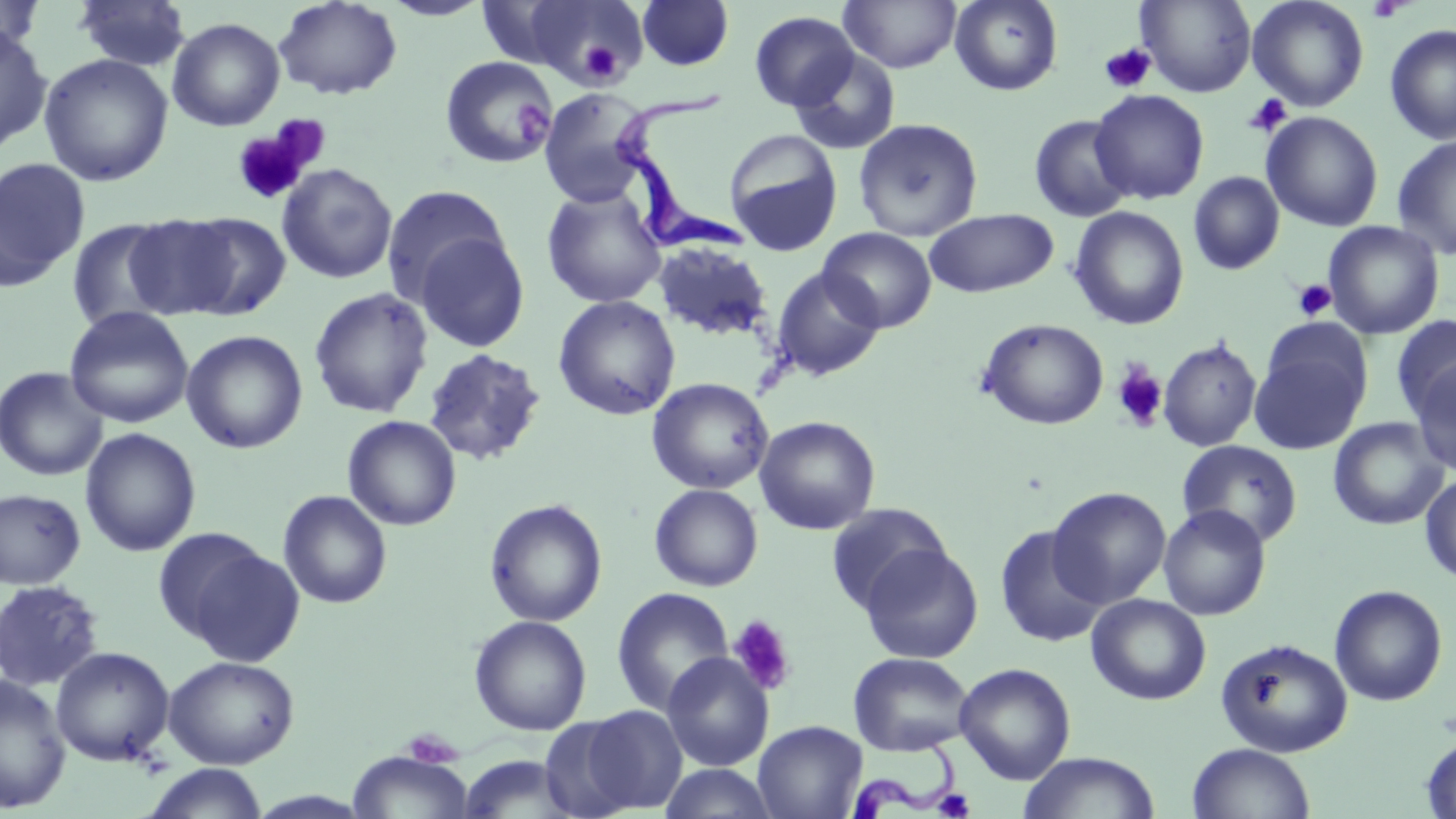
Approximate bounding boxes as (x1,y1)-(x2,y2) corner pairs in pixels. Platelet locations: (1366,0)-(1411,22), (575,38)-(623,83), (1099,44)-(1156,93), (1244,94)-(1291,137), (512,101)-(553,143), (231,121)-(320,206), (1292,279)-(1337,321), (1111,361)-(1168,432), (727,615)-(797,697), (932,788)-(976,818). Uninfected red blood cell locations: (0,0)-(43,61), (273,0)-(403,100), (380,0)-(494,20), (637,0)-(734,70), (839,0)-(962,74), (949,0)-(1063,96), (1136,0)-(1257,97), (1247,0)-(1369,112), (73,1)-(190,72), (523,2)-(648,90), (749,11)-(859,111), (167,17)-(285,132), (0,22)-(53,155), (1385,24)-(1456,144), (789,49)-(901,155), (39,53)-(174,186), (440,55)-(555,170), (538,87)-(653,207), (1090,89)-(1210,204), (1261,111)-(1384,232), (1029,115)-(1134,222), (853,118)-(983,241), (724,130)-(843,255), (1392,133)-(1456,261), (0,158)-(89,291), (276,164)-(397,284), (1188,171)-(1285,275), (381,185)-(512,306), (541,186)-(666,308), (1069,206)-(1190,330), (924,209)-(1058,298), (172,212)-(292,320), (128,217)-(240,321), (68,219)-(179,333), (1323,221)-(1444,340), (818,227)-(937,332), (411,230)-(530,353), (652,242)-(775,343), (771,266)-(885,382), (309,287)-(434,419), (553,295)-(680,420), (64,306)-(194,429), (1391,315)-(1456,424), (977,318)-(1109,430), (1260,318)-(1374,409), (181,330)-(308,454), (1157,338)-(1262,452), (1250,347)-(1366,455), (422,348)-(547,466), (1409,360)-(1456,476), (0,366)-(108,481), (646,377)-(774,494), (342,415)-(462,531), (754,416)-(880,535), (1328,417)-(1449,530), (80,427)-(201,557), (1177,439)-(1302,547), (1420,473)-(1456,585), (649,484)-(763,592), (1048,487)-(1172,608), (0,489)-(86,590), (278,490)-(392,609), (484,499)-(608,627), (825,503)-(953,616), (1158,504)-(1271,621), (994,524)-(1108,648), (157,530)-(301,663), (858,543)-(983,664), (0,579)-(105,692), (1330,585)-(1448,706), (611,586)-(734,717), (1086,594)-(1211,705), (469,615)-(592,735), (1216,637)-(1353,758), (50,646)-(175,766), (849,652)-(975,756), (661,653)-(774,771), (164,655)-(300,769), (954,662)-(1076,784), (0,675)-(71,812), (573,705)-(688,815), (753,720)-(867,819), (1421,734)-(1456,818), (1186,743)-(1316,819), (347,749)-(474,819), (1018,751)-(1159,819), (456,755)-(579,818), (142,763)-(269,819), (658,763)-(781,819). Trypanosoma brucei locations: (615,84)-(757,260), (405,730)-(457,765), (851,737)-(964,818). Slide-level diagnosis: Trypanosoma brucei. Thin blood smear. May-Grünwald-Giemsa stain. One field of a larger specimen. Image is 1456×819 pixels. Captured at 1000x magnification. Optical microscopy.